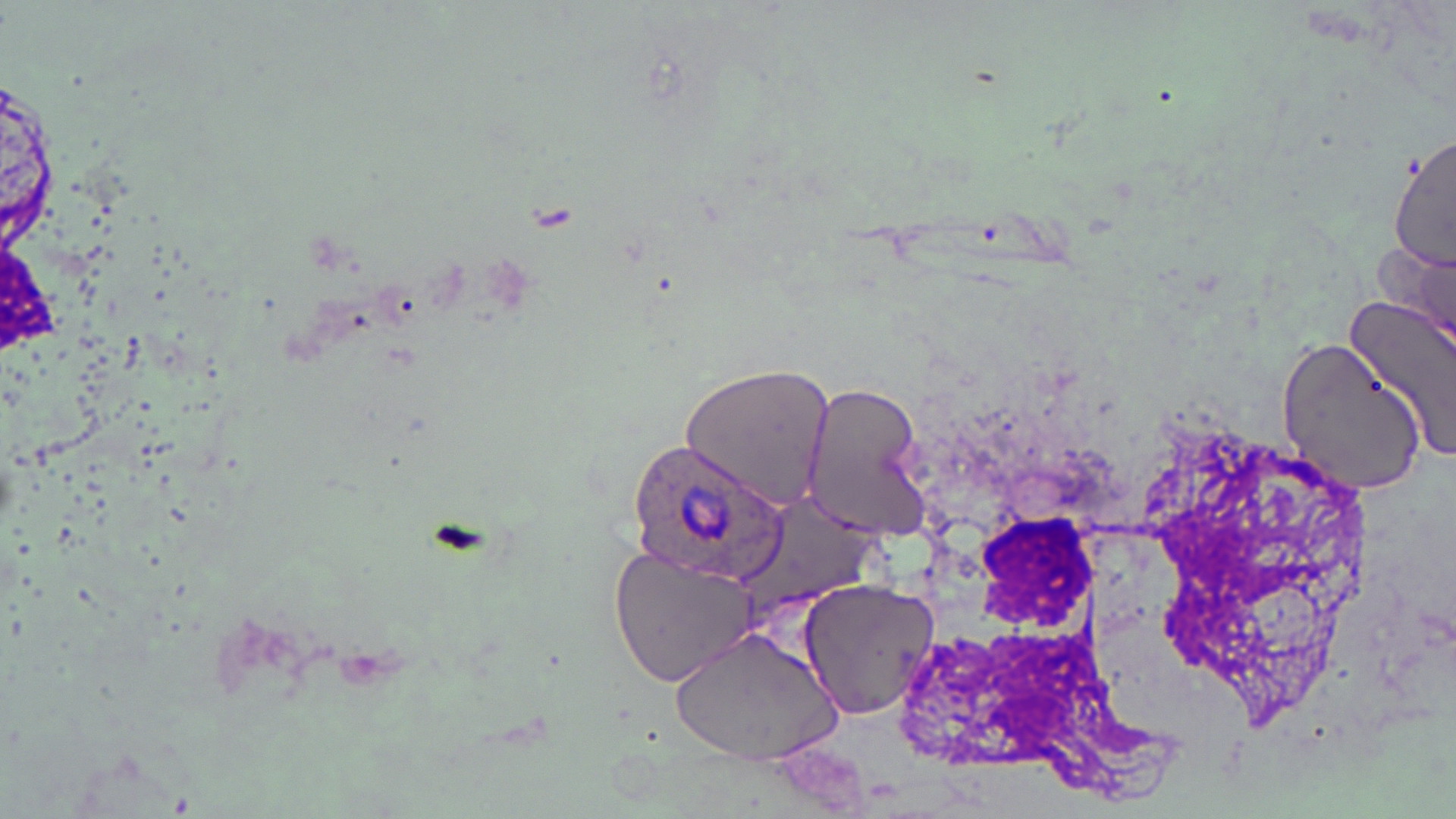 Approximate bounding boxes as [x1, y1, x2, y2] in pixels. Plasmodium ovale-infected red blood cell locations: [629, 440, 785, 584]. Uninfected red blood cell locations: [1389, 129, 1455, 276], [1373, 241, 1454, 339], [1344, 292, 1456, 461], [1273, 336, 1430, 497], [679, 361, 837, 512], [800, 382, 929, 540], [610, 544, 761, 689], [795, 575, 941, 722], [671, 627, 840, 767]. Slide-level diagnosis: Plasmodium ovale. 1000x magnification. May-Grünwald-Giemsa-stained preparation. Single field of view. Image is 1456×819 pixels. Optical microscopy. Thin blood smear.